Identify the parasite.
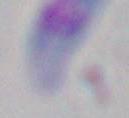
This is Toxoplasma gondii.

Summary:
  - Modality: micrograph
  - Magnification: 1000x